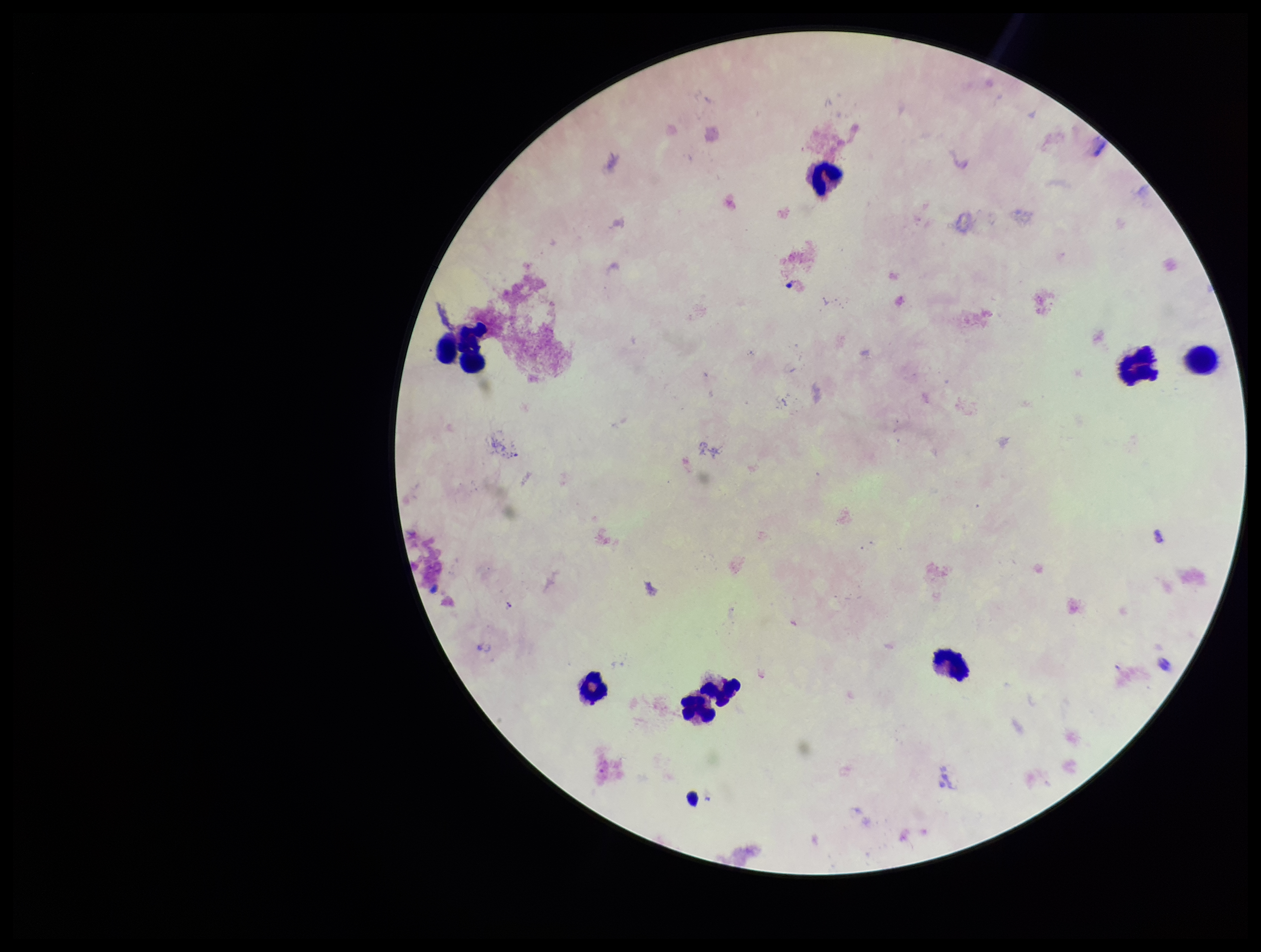
Plasmodium parasites: none detected. Smartphone photograph taken through the eyepiece of a microscope. Giemsa stain. Preparation: thick blood smear. Image is 1261×952 pixels. Patient malaria status: positive. Parasite count: 0. Single field of view. Species reported for this patient: Plasmodium falciparum. Leukocyte count: 9.